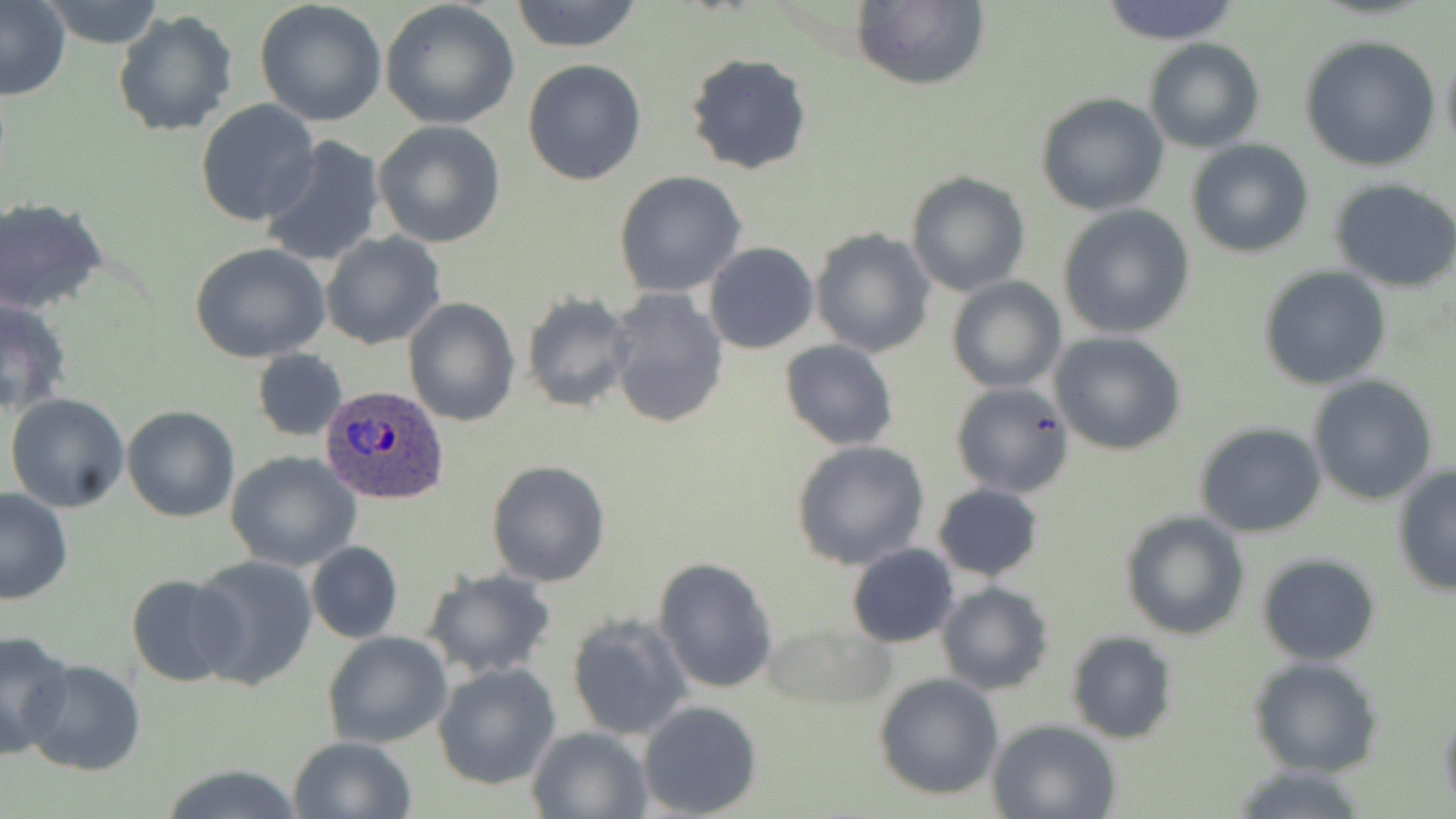

Summary:
  - Coordinate format: approximate bounding boxes as (x1,y1)-(x2,y2) corner pairs in pixels
  - Plasmodium ovale-infected red blood cell locations: (318,385)-(450,505)
  - Uninfected red blood cell locations: (0,0)-(70,102), (42,0)-(167,48), (510,0)-(643,52), (254,1)-(388,125), (851,1)-(990,91), (1095,1)-(1244,46), (380,2)-(520,132), (112,10)-(237,136), (1299,35)-(1442,172), (1144,39)-(1264,152), (1440,39)-(1456,163), (685,54)-(813,176), (522,58)-(648,186), (1034,91)-(1169,216), (195,100)-(322,228), (373,120)-(507,248), (260,137)-(386,268), (1186,138)-(1314,258), (906,170)-(1032,297), (614,171)-(746,297), (1329,178)-(1456,293), (1,198)-(112,316), (1057,206)-(1195,339), (810,228)-(935,357), (321,232)-(446,350), (703,241)-(819,354), (189,244)-(333,364), (1260,266)-(1389,388), (947,278)-(1065,392), (607,288)-(730,430), (520,291)-(635,413), (0,297)-(72,418), (403,297)-(520,428), (1049,332)-(1187,456), (780,340)-(898,451), (252,349)-(346,441), (1306,376)-(1439,505), (951,381)-(1073,497), (5,393)-(131,513), (121,405)-(239,523), (1195,423)-(1326,537), (791,442)-(931,570), (226,451)-(363,571), (487,460)-(611,586), (1392,465)-(1456,597), (933,483)-(1043,582), (0,487)-(74,604), (1120,510)-(1249,640), (306,541)-(402,643), (847,544)-(961,648), (1257,553)-(1382,664), (188,554)-(319,690), (653,556)-(779,693), (422,568)-(557,678), (125,573)-(240,687), (937,582)-(1053,696), (567,614)-(692,742), (761,623)-(896,715), (0,630)-(75,760), (1067,631)-(1178,744), (322,632)-(453,748), (1249,657)-(1384,778), (22,658)-(145,774), (433,664)-(562,789), (873,673)-(1003,801), (637,700)-(763,818), (1438,705)-(1456,811), (987,718)-(1122,819), (526,726)-(653,818), (287,736)-(417,819), (161,763)-(305,819), (1227,765)-(1373,819)
  - Slide-level diagnosis: Plasmodium ovale
  - Image size: 1456×819 pixels
  - Field of view: one of a larger specimen
  - Stain: May-Grünwald-Giemsa
  - Modality: light microscopy
  - Magnification: 1000x
  - Preparation: thin blood smear